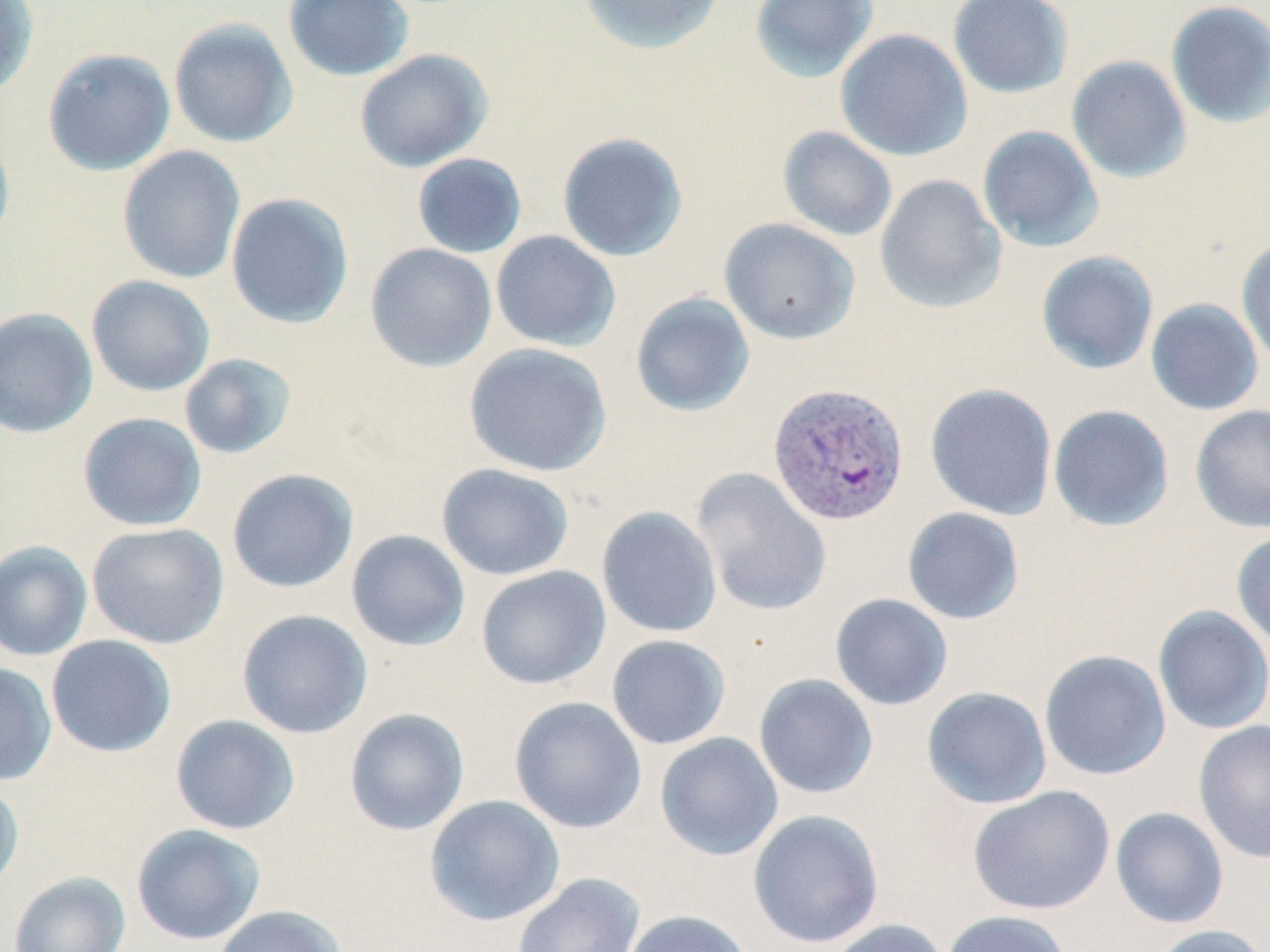

slide-level diagnosis = Plasmodium vivax
image size = 1270×952 pixels
preparation = thin blood film
stain = May-Grünwald-Giemsa
modality = light microscopy
field of view = single
uninfected red blood cell locations = approximate bounding boxes as (x1, y1, x2, y2) in pixels: (283, 0, 414, 81), (576, 0, 725, 56), (749, 0, 877, 84), (948, 0, 1074, 99), (1165, 0, 1270, 128), (0, 1, 39, 101), (168, 18, 298, 148), (835, 29, 973, 161), (41, 47, 176, 177), (354, 48, 492, 172), (1066, 55, 1192, 183), (977, 125, 1103, 252), (0, 126, 15, 253), (778, 126, 898, 242), (557, 131, 689, 262), (117, 145, 245, 284), (411, 152, 528, 258), (874, 173, 1007, 314), (225, 192, 354, 329), (719, 217, 860, 345), (490, 230, 621, 352), (1236, 237, 1270, 371), (365, 242, 498, 372), (1035, 250, 1159, 375), (86, 274, 216, 397), (630, 292, 755, 417), (1145, 298, 1264, 416), (0, 307, 98, 439), (464, 342, 612, 477), (179, 353, 297, 460), (924, 382, 1057, 520), (1048, 404, 1175, 531), (1190, 404, 1270, 533), (78, 412, 207, 532), (435, 463, 574, 581), (691, 467, 832, 616), (226, 468, 358, 593), (597, 506, 722, 638), (902, 507, 1025, 625), (86, 522, 229, 649), (346, 529, 470, 651), (1231, 529, 1270, 653), (0, 540, 93, 661), (476, 565, 611, 690), (830, 593, 953, 711), (1152, 605, 1270, 734), (237, 609, 373, 739), (607, 634, 731, 750), (46, 635, 177, 757), (1039, 649, 1171, 781), (0, 663, 57, 786), (753, 673, 879, 799), (921, 686, 1053, 809), (509, 696, 647, 833), (344, 708, 470, 835), (170, 714, 300, 835), (1193, 719, 1270, 864), (654, 732, 784, 861), (0, 777, 25, 897), (967, 785, 1115, 915), (424, 795, 566, 926), (1110, 807, 1229, 929), (747, 809, 885, 949), (131, 823, 266, 945), (9, 871, 131, 952), (512, 872, 645, 952), (213, 905, 346, 952), (621, 909, 755, 952), (939, 910, 1073, 952), (825, 918, 950, 952), (1147, 924, 1267, 952)
magnification = 1000x
Plasmodium vivax-infected red blood cell locations = approximate bounding boxes as (x1, y1, x2, y2) in pixels: (767, 381, 910, 527)